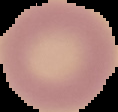
From a thin blood film. The area outside the segmented cell region is set to black. Result: no Plasmodium parasites seen. Image is 118×112 pixels.